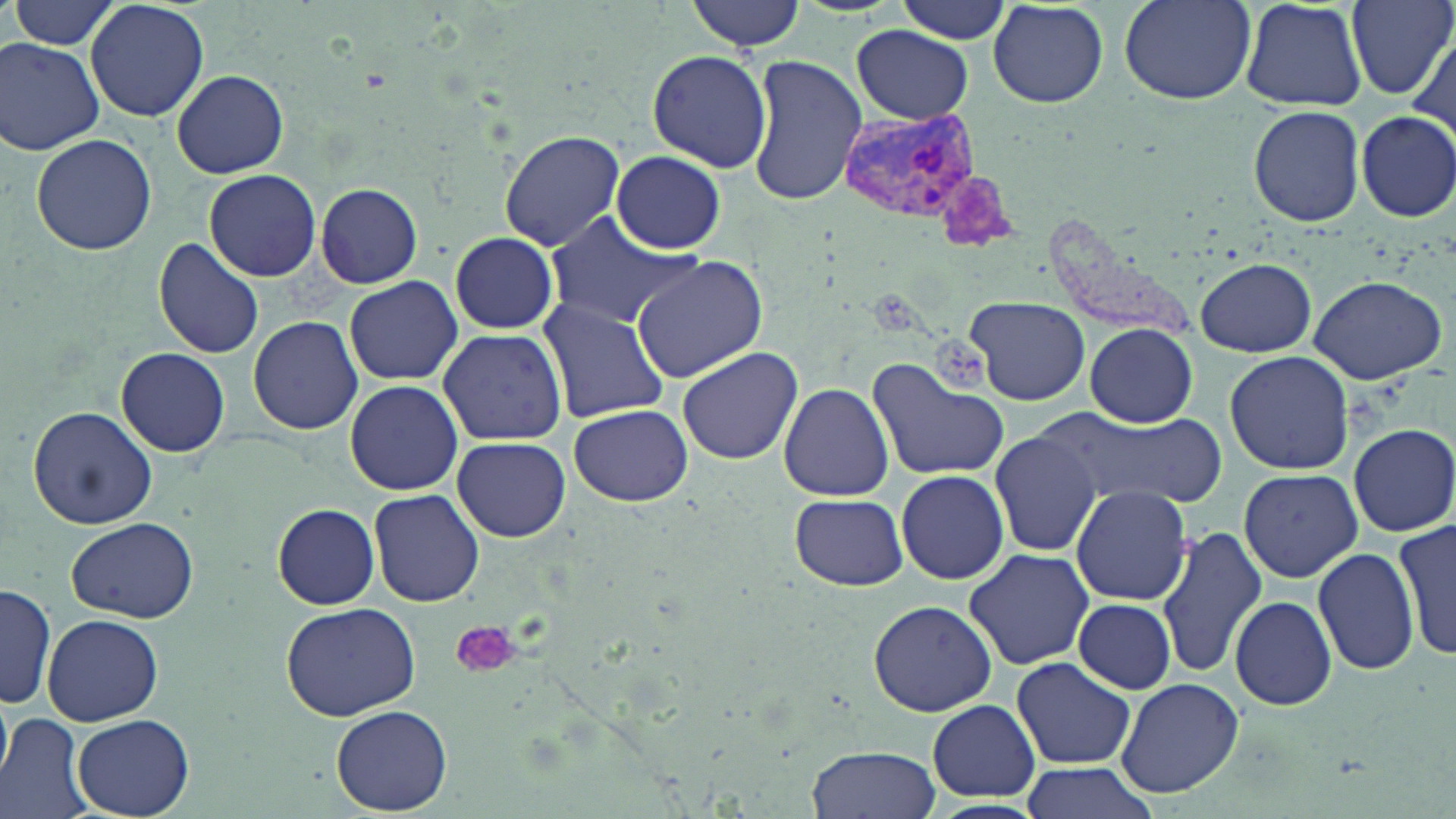
slide-level diagnosis = Plasmodium vivax
field of view = single
uninfected red blood cell locations = approximate bounding boxes as (x1, y1, x2, y2) in pixels: (9, 0, 123, 52), (86, 0, 211, 122), (687, 0, 805, 53), (1119, 0, 1256, 104), (1239, 0, 1368, 112), (1344, 0, 1455, 100), (896, 1, 1016, 44), (990, 2, 1108, 108), (8, 22, 183, 143), (850, 24, 975, 124), (0, 36, 104, 155), (1409, 38, 1453, 142), (646, 50, 773, 173), (745, 54, 868, 205), (171, 70, 289, 179), (1249, 105, 1365, 227), (1355, 110, 1456, 223), (31, 132, 157, 256), (499, 132, 624, 250), (609, 151, 727, 253), (204, 170, 321, 281), (315, 182, 423, 289), (548, 213, 704, 328), (450, 231, 557, 335), (153, 236, 264, 360), (630, 255, 769, 386), (1196, 257, 1317, 355), (1308, 273, 1447, 385), (345, 276, 461, 386), (963, 294, 1091, 405), (537, 296, 668, 423), (249, 316, 362, 434), (1083, 324, 1199, 426), (436, 325, 567, 446), (676, 347, 803, 463), (117, 348, 230, 456), (1224, 351, 1354, 475), (870, 360, 1008, 479), (345, 380, 463, 496), (778, 382, 894, 501), (568, 404, 693, 507), (28, 405, 157, 530), (1044, 412, 1224, 504), (1349, 423, 1456, 536), (991, 430, 1099, 556), (452, 436, 571, 542), (1238, 468, 1362, 582), (896, 470, 1011, 585), (1070, 485, 1193, 605), (369, 489, 482, 605), (789, 494, 908, 591), (272, 504, 381, 608), (67, 516, 198, 622), (1395, 517, 1456, 660), (1156, 527, 1268, 681), (1314, 546, 1420, 678), (962, 547, 1096, 670), (1, 578, 58, 714), (1230, 596, 1338, 711), (869, 598, 997, 716), (1075, 598, 1176, 692), (278, 601, 422, 719), (42, 613, 164, 726), (1011, 656, 1136, 769), (1116, 678, 1244, 799), (0, 694, 13, 785), (927, 699, 1040, 803), (333, 706, 451, 815), (0, 712, 92, 819), (72, 713, 195, 817), (806, 747, 942, 819), (1016, 760, 1162, 819)
magnification = 1000x
stain = May-Grünwald-Giemsa
modality = light microscopy
platelet locations = approximate bounding boxes as (x1, y1, x2, y2) in pixels: (449, 621, 519, 679)
Plasmodium vivax-infected red blood cell locations = approximate bounding boxes as (x1, y1, x2, y2) in pixels: (837, 107, 985, 231)
preparation = thin blood smear
image size = 1456×819 pixels